Name the blood parasite species.
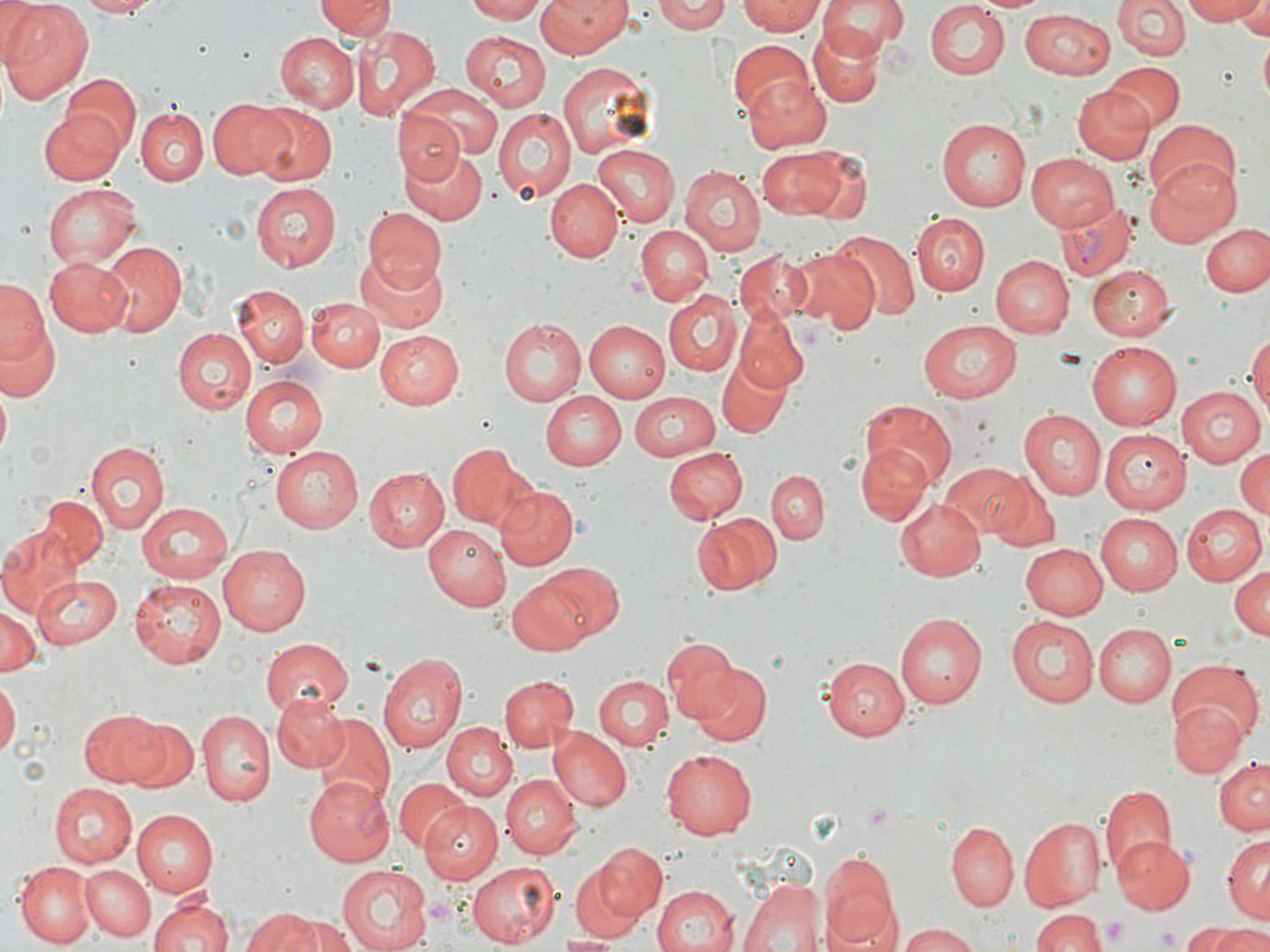
Plasmodium vivax.

Approximate bounding boxes as named x1/y1/x2/y2 corners in pixels. Platelet locations: (x1=864, y1=804, x2=892, y2=829), (x1=1103, y1=915, x2=1128, y2=944), (x1=1154, y1=924, x2=1182, y2=951). Uninfected red blood cell locations: (x1=1, y1=0, x2=46, y2=65), (x1=1, y1=0, x2=94, y2=104), (x1=73, y1=0, x2=161, y2=16), (x1=317, y1=0, x2=394, y2=42), (x1=462, y1=0, x2=545, y2=22), (x1=536, y1=0, x2=631, y2=59), (x1=652, y1=0, x2=734, y2=34), (x1=738, y1=0, x2=826, y2=35), (x1=820, y1=0, x2=907, y2=56), (x1=979, y1=0, x2=1046, y2=14), (x1=1182, y1=0, x2=1265, y2=25), (x1=923, y1=1, x2=1009, y2=81), (x1=1113, y1=1, x2=1190, y2=61), (x1=1231, y1=4, x2=1270, y2=36), (x1=1020, y1=9, x2=1116, y2=77), (x1=358, y1=25, x2=440, y2=122), (x1=808, y1=26, x2=884, y2=107), (x1=461, y1=29, x2=554, y2=110), (x1=276, y1=30, x2=358, y2=110), (x1=1258, y1=36, x2=1269, y2=109), (x1=726, y1=38, x2=811, y2=117), (x1=557, y1=62, x2=653, y2=158), (x1=1106, y1=62, x2=1186, y2=128), (x1=742, y1=74, x2=833, y2=153), (x1=61, y1=75, x2=140, y2=156), (x1=406, y1=84, x2=504, y2=163), (x1=1071, y1=86, x2=1153, y2=164), (x1=208, y1=99, x2=291, y2=179), (x1=249, y1=104, x2=336, y2=185), (x1=40, y1=106, x2=128, y2=184), (x1=492, y1=107, x2=576, y2=203), (x1=136, y1=109, x2=206, y2=187), (x1=394, y1=110, x2=464, y2=186), (x1=939, y1=117, x2=1034, y2=211), (x1=1145, y1=118, x2=1241, y2=204), (x1=594, y1=143, x2=681, y2=224), (x1=401, y1=145, x2=489, y2=224), (x1=756, y1=147, x2=850, y2=219), (x1=803, y1=149, x2=870, y2=222), (x1=1026, y1=152, x2=1117, y2=231), (x1=1145, y1=156, x2=1242, y2=246), (x1=678, y1=167, x2=764, y2=256), (x1=545, y1=179, x2=623, y2=262), (x1=43, y1=181, x2=140, y2=270), (x1=250, y1=181, x2=340, y2=272), (x1=361, y1=208, x2=449, y2=290), (x1=914, y1=213, x2=989, y2=294), (x1=635, y1=223, x2=714, y2=305), (x1=1202, y1=224, x2=1270, y2=296), (x1=830, y1=228, x2=920, y2=323), (x1=95, y1=241, x2=185, y2=338), (x1=788, y1=246, x2=878, y2=332), (x1=733, y1=251, x2=813, y2=327), (x1=355, y1=252, x2=448, y2=335), (x1=992, y1=254, x2=1073, y2=337), (x1=43, y1=256, x2=134, y2=336), (x1=1089, y1=265, x2=1176, y2=341), (x1=0, y1=278, x2=47, y2=364), (x1=234, y1=282, x2=309, y2=368), (x1=665, y1=292, x2=741, y2=376), (x1=305, y1=295, x2=382, y2=372), (x1=733, y1=307, x2=810, y2=392), (x1=4, y1=318, x2=61, y2=403), (x1=499, y1=318, x2=586, y2=405), (x1=582, y1=319, x2=670, y2=401), (x1=917, y1=319, x2=1022, y2=401), (x1=171, y1=329, x2=255, y2=415), (x1=375, y1=329, x2=463, y2=408), (x1=1246, y1=331, x2=1270, y2=425), (x1=1087, y1=343, x2=1181, y2=429), (x1=718, y1=356, x2=789, y2=439), (x1=240, y1=374, x2=327, y2=457), (x1=1174, y1=383, x2=1268, y2=467), (x1=628, y1=390, x2=722, y2=459), (x1=540, y1=392, x2=624, y2=469), (x1=862, y1=397, x2=957, y2=489), (x1=1020, y1=407, x2=1108, y2=499), (x1=1103, y1=428, x2=1192, y2=513), (x1=86, y1=439, x2=169, y2=533), (x1=446, y1=441, x2=533, y2=532), (x1=858, y1=443, x2=930, y2=524), (x1=271, y1=445, x2=367, y2=533), (x1=662, y1=445, x2=749, y2=523), (x1=1233, y1=446, x2=1270, y2=522), (x1=455, y1=447, x2=576, y2=559), (x1=942, y1=464, x2=1033, y2=537), (x1=361, y1=466, x2=447, y2=552), (x1=768, y1=470, x2=828, y2=544), (x1=987, y1=476, x2=1060, y2=553), (x1=493, y1=486, x2=579, y2=571), (x1=37, y1=496, x2=108, y2=572), (x1=136, y1=500, x2=233, y2=582), (x1=895, y1=500, x2=987, y2=582), (x1=1178, y1=503, x2=1265, y2=587), (x1=1093, y1=512, x2=1182, y2=596), (x1=692, y1=515, x2=775, y2=595), (x1=422, y1=525, x2=510, y2=611), (x1=0, y1=529, x2=80, y2=615), (x1=1022, y1=543, x2=1109, y2=620), (x1=218, y1=546, x2=310, y2=634), (x1=541, y1=562, x2=625, y2=641), (x1=1228, y1=565, x2=1270, y2=641), (x1=34, y1=574, x2=123, y2=649), (x1=506, y1=575, x2=595, y2=658), (x1=130, y1=578, x2=227, y2=669), (x1=0, y1=608, x2=42, y2=676), (x1=896, y1=613, x2=985, y2=709), (x1=1006, y1=616, x2=1098, y2=708), (x1=1093, y1=622, x2=1176, y2=704), (x1=263, y1=636, x2=354, y2=717), (x1=663, y1=636, x2=740, y2=717), (x1=377, y1=653, x2=467, y2=754), (x1=822, y1=656, x2=910, y2=741), (x1=1166, y1=659, x2=1263, y2=746), (x1=689, y1=662, x2=770, y2=744), (x1=500, y1=675, x2=577, y2=752), (x1=595, y1=675, x2=672, y2=751), (x1=0, y1=682, x2=18, y2=761), (x1=272, y1=693, x2=350, y2=774), (x1=1171, y1=701, x2=1248, y2=777), (x1=78, y1=709, x2=169, y2=786), (x1=195, y1=710, x2=274, y2=806), (x1=311, y1=713, x2=394, y2=807), (x1=111, y1=714, x2=197, y2=790), (x1=443, y1=722, x2=518, y2=800), (x1=550, y1=729, x2=632, y2=811), (x1=661, y1=749, x2=757, y2=839), (x1=1213, y1=760, x2=1270, y2=835), (x1=499, y1=773, x2=579, y2=859), (x1=301, y1=777, x2=394, y2=865), (x1=396, y1=779, x2=473, y2=855), (x1=48, y1=783, x2=137, y2=868), (x1=1100, y1=783, x2=1178, y2=874), (x1=422, y1=803, x2=503, y2=884), (x1=132, y1=808, x2=218, y2=895), (x1=1020, y1=816, x2=1105, y2=909), (x1=946, y1=820, x2=1018, y2=910), (x1=1223, y1=835, x2=1269, y2=923), (x1=1112, y1=836, x2=1192, y2=914), (x1=594, y1=843, x2=666, y2=920), (x1=820, y1=856, x2=898, y2=950), (x1=14, y1=859, x2=95, y2=947), (x1=465, y1=860, x2=560, y2=946), (x1=570, y1=861, x2=650, y2=940), (x1=335, y1=864, x2=431, y2=952), (x1=79, y1=865, x2=156, y2=941), (x1=739, y1=876, x2=824, y2=952), (x1=649, y1=883, x2=741, y2=952), (x1=149, y1=895, x2=231, y2=952), (x1=241, y1=908, x2=324, y2=952), (x1=1032, y1=908, x2=1108, y2=952), (x1=288, y1=913, x2=358, y2=952), (x1=895, y1=922, x2=983, y2=952), (x1=1181, y1=925, x2=1244, y2=951), (x1=1211, y1=925, x2=1270, y2=952), (x1=559, y1=934, x2=616, y2=950). Plasmodium vivax-infected red blood cell locations: (x1=1058, y1=198, x2=1137, y2=281). May-Grünwald-Giemsa-stained preparation. Light microscopy. Captured at 1000x magnification. Image is 1270×952 pixels. One field of a larger specimen. Thin blood film.